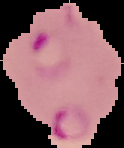

malaria status = parasitized
image type = segmented cell region on a black background
preparation = thin blood smear
image size = 124×148 pixels